Outline each blood parasite and name the species.
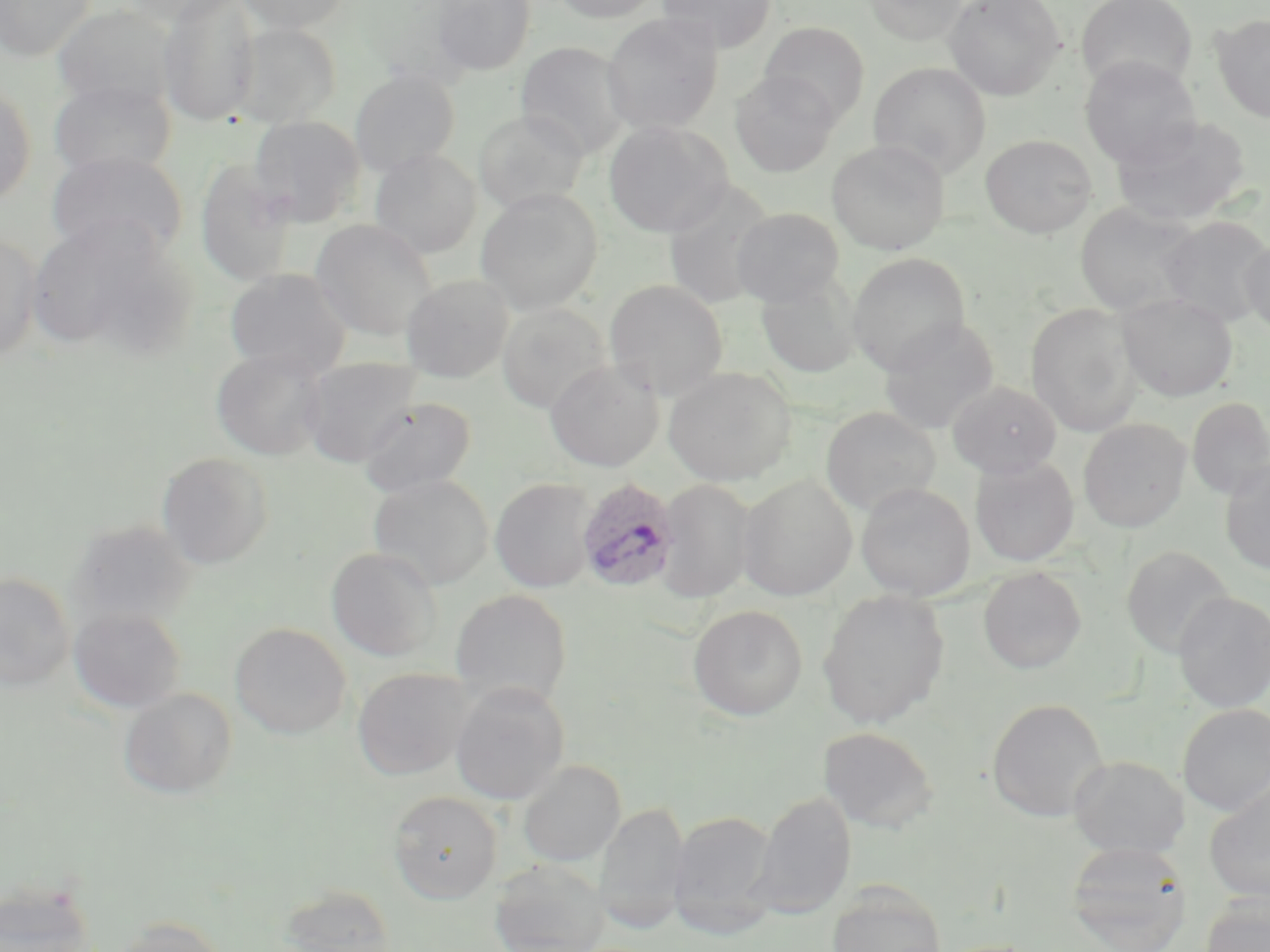

Approximate bounding boxes as [x1, y1, x2, y2] in pixels.
Plasmodium ovale-infected red blood cells: [575, 477, 680, 593].
No Plasmodium falciparum, Plasmodium malariae, Plasmodium vivax, Babesia divergens, or Trypanosoma brucei observed.

Summary:
  - Uninfected red blood cell locations: [1, 0, 97, 60], [122, 0, 243, 26], [157, 0, 262, 126], [235, 0, 351, 33], [430, 0, 536, 75], [551, 0, 663, 23], [657, 0, 776, 52], [863, 0, 968, 46], [944, 0, 1065, 99], [1076, 0, 1198, 94], [51, 3, 178, 112], [602, 13, 723, 135], [1211, 13, 1270, 124], [232, 21, 341, 126], [759, 21, 870, 125], [515, 41, 632, 159], [1079, 56, 1201, 168], [868, 62, 990, 178], [349, 70, 460, 176], [730, 70, 840, 177], [48, 79, 176, 180], [0, 82, 36, 206], [474, 109, 588, 214], [1111, 114, 1252, 227], [249, 116, 365, 226], [603, 120, 731, 237], [981, 134, 1097, 238], [827, 140, 950, 255], [369, 149, 482, 258], [47, 151, 189, 264], [195, 160, 300, 285], [662, 181, 777, 309], [475, 188, 602, 315], [1074, 202, 1203, 317], [731, 207, 845, 307], [25, 216, 193, 362], [1159, 216, 1270, 327], [310, 219, 438, 341], [0, 234, 42, 364], [1241, 235, 1270, 337], [847, 252, 971, 374], [224, 268, 352, 377], [400, 274, 514, 382], [755, 275, 862, 378], [604, 279, 728, 399], [1118, 293, 1237, 401], [497, 304, 612, 413], [1026, 304, 1142, 436], [879, 317, 1000, 435], [211, 348, 330, 461], [300, 358, 421, 468], [544, 360, 664, 472], [664, 366, 796, 485], [948, 380, 1062, 478], [358, 397, 476, 497], [1186, 397, 1270, 499], [821, 406, 941, 516], [1078, 418, 1191, 532], [157, 451, 273, 569], [970, 456, 1080, 566], [1220, 460, 1270, 574], [367, 473, 494, 590], [737, 475, 857, 600], [490, 477, 597, 593], [658, 478, 756, 603], [856, 483, 975, 601], [67, 520, 196, 629], [1121, 546, 1234, 659], [326, 547, 443, 661], [978, 566, 1086, 674], [0, 572, 75, 692], [450, 589, 572, 707], [817, 589, 950, 728], [1173, 591, 1270, 712], [688, 604, 807, 721], [68, 607, 187, 713], [230, 622, 351, 739], [352, 666, 473, 780], [450, 681, 569, 805], [119, 687, 237, 799], [987, 698, 1109, 821], [1178, 703, 1270, 815], [819, 726, 939, 833], [1068, 755, 1187, 860], [517, 760, 625, 866], [1203, 779, 1270, 903], [388, 790, 502, 903], [751, 791, 856, 918], [596, 802, 689, 932], [668, 810, 779, 933], [1065, 840, 1192, 952], [489, 858, 609, 952], [1, 879, 98, 952], [826, 884, 947, 952], [280, 885, 398, 951], [1201, 894, 1270, 952], [111, 917, 227, 952]
  - Slide-level diagnosis: Plasmodium ovale
  - Preparation: thin blood film
  - Field of view: single
  - Magnification: 1000x
  - Stain: May-Grünwald-Giemsa
  - Modality: light microscopy
  - Image size: 1270×952 pixels